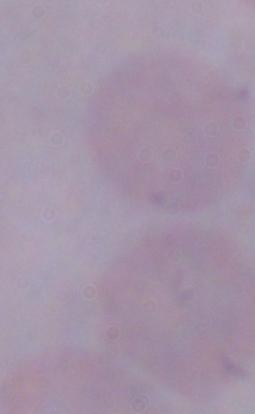

Summary:
  - Identification: trypanosome
  - Modality: micrograph
  - Magnification: 1000x